Assess the morphology of the red blood cells.
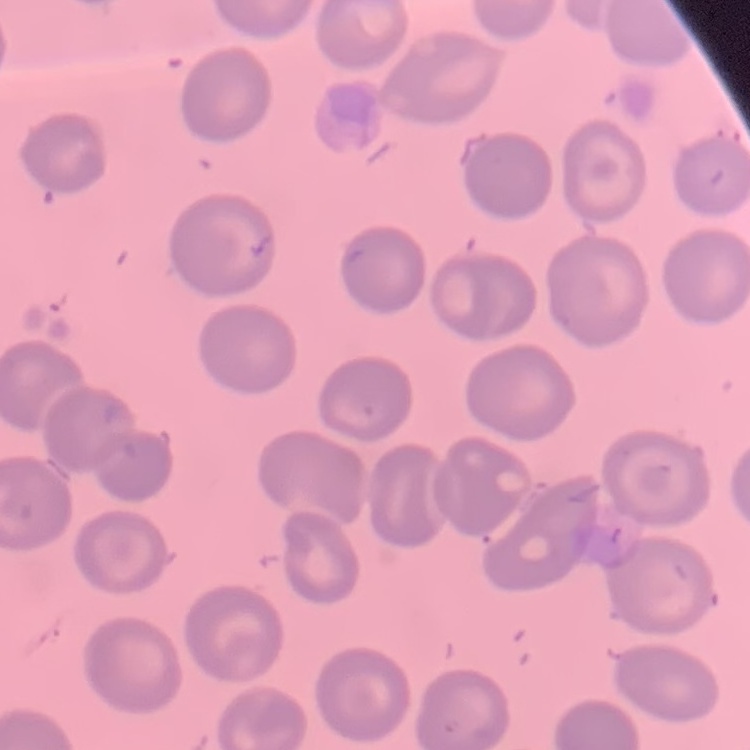
They show no rouleaux formation.

preparation = thin blood smear
image type = square crop of a larger photomicrograph
stain = Field's or Giemsa